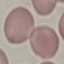
result: negative for malaria parasites
preparation: thin blood film
capture: smartphone camera at the microscope eyepiece
image_type: automatically extracted cell patch, resized to 64 × 64 pixels
stain: Giemsa